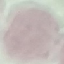

Malaria status: uninfected. Automatically extracted cell patch, resized to 64 × 64 pixels. Thin blood smear. Acquired by smartphone through the microscope eyepiece. Giemsa-stained preparation.